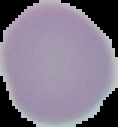
Segmented cell region on a black background. From a thin blood smear. Result: negative for Plasmodium parasites. Image is 118×127 pixels.